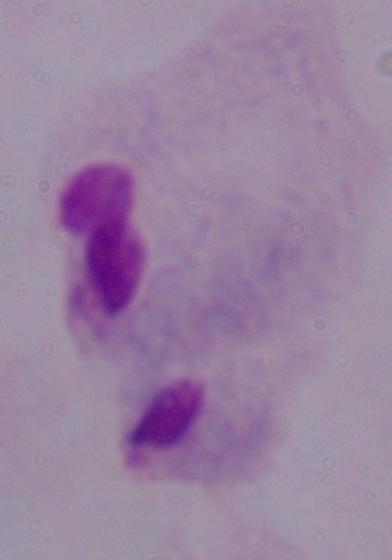

Summary:
  - Modality: micrograph
  - Identification: trichomonad
  - Magnification: 1000x